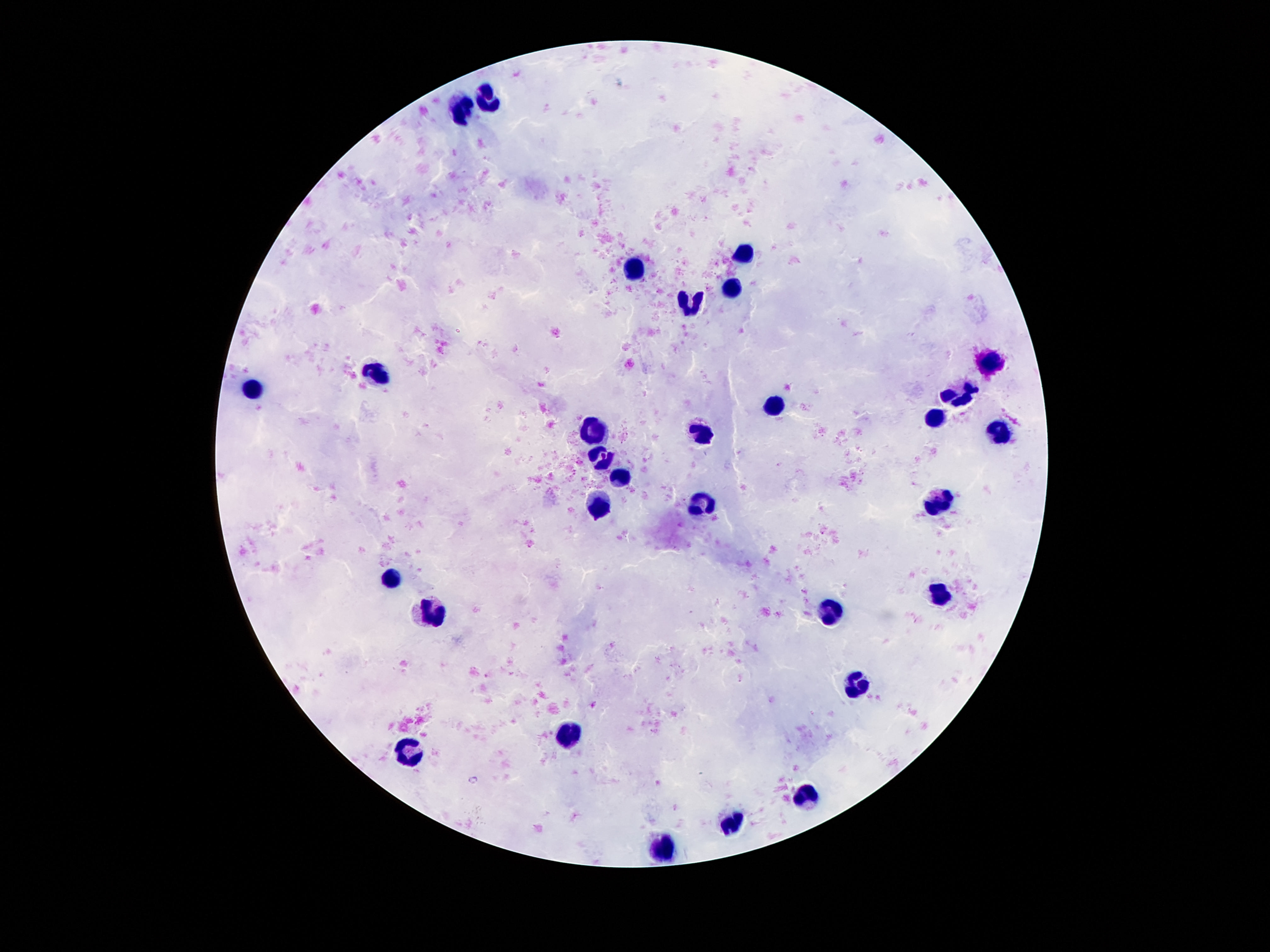
capture = smartphone camera through the microscope eyepiece
magnification = 100x
field of view = single
stain = Giemsa
leukocyte locations = approximate centers as (x, y) in pixels: (484, 99), (462, 110), (746, 251), (633, 269), (732, 288), (692, 304), (989, 362), (376, 372), (252, 388), (958, 397), (774, 406), (936, 417), (597, 428), (706, 435), (1000, 435), (602, 457), (619, 475), (602, 503), (942, 503), (699, 505), (392, 581), (942, 595), (832, 612), (434, 618), (856, 684), (566, 737), (407, 754), (807, 798), (730, 823), (666, 848)
patient malaria status = negative
image size = 1270×952 pixels
preparation = thick peripheral-blood smear